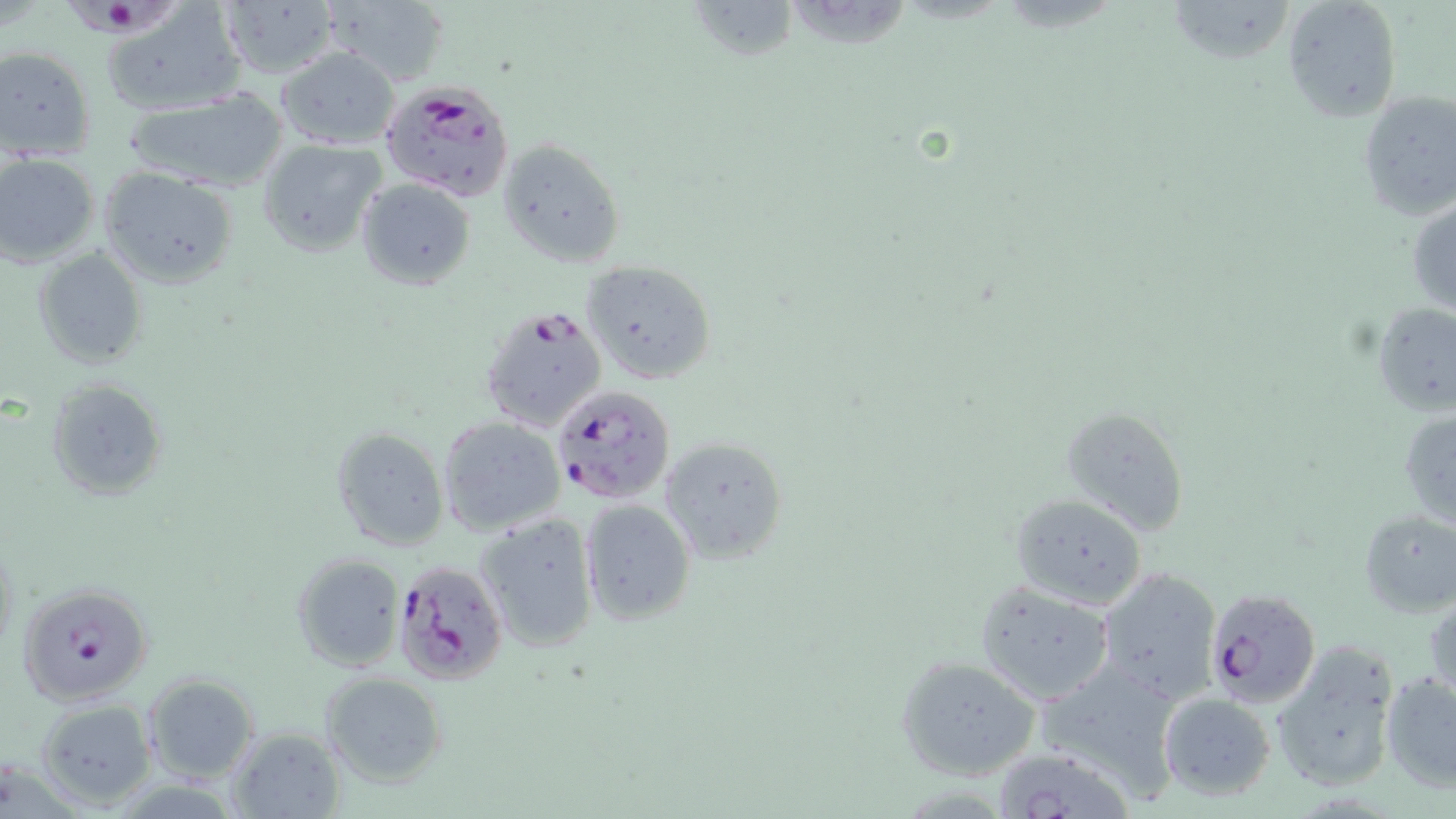
Approximate bounding boxes as (x1, y1, x2, y2) in pixels. Uninfected red blood cell locations: (322, 0, 450, 87), (688, 0, 799, 60), (1167, 0, 1295, 69), (215, 1, 335, 79), (1282, 1, 1401, 122), (103, 3, 244, 116), (0, 46, 95, 160), (275, 47, 400, 149), (1355, 88, 1456, 222), (123, 89, 290, 192), (496, 137, 625, 269), (259, 140, 385, 257), (0, 153, 100, 268), (99, 166, 239, 290), (356, 178, 475, 291), (1408, 195, 1456, 317), (33, 248, 147, 368), (579, 259, 716, 385), (1373, 303, 1456, 415), (46, 379, 167, 503), (436, 404, 682, 521), (1058, 406, 1191, 535), (1399, 406, 1456, 530), (436, 416, 566, 536), (331, 425, 450, 553), (657, 435, 787, 564), (1010, 492, 1148, 608), (580, 499, 698, 626), (1358, 509, 1456, 619), (474, 511, 600, 654), (291, 553, 406, 671), (1094, 567, 1220, 704), (975, 580, 1114, 705), (1427, 589, 1456, 711), (1272, 639, 1402, 795), (895, 656, 1041, 782), (1030, 661, 1186, 803), (1379, 671, 1456, 792), (321, 673, 448, 789), (142, 674, 260, 785), (1159, 692, 1274, 802), (36, 699, 155, 809), (226, 726, 345, 817), (991, 745, 1140, 819). Plasmodium falciparum-infected red blood cell locations: (65, 0, 177, 38), (381, 80, 515, 202), (478, 300, 608, 432), (549, 382, 676, 503), (393, 558, 508, 684), (15, 580, 151, 706), (1204, 588, 1322, 707). Slide-level diagnosis: Plasmodium falciparum. May-Grünwald-Giemsa stain. Thin blood smear. Image is 1456×819 pixels. Single field of view. Captured at 1000x magnification. Light microscopy.